Report the malaria status of this cell.
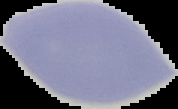
Uninfected.

preparation: thin blood film
image_type: segmented cell region with the area outside set to black
image_size: 178×109 pixels